Identify the parasite.
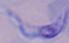
A trypanosome.

Summary:
  - Modality: micrograph
  - Magnification: 1000x